Identify the cell.
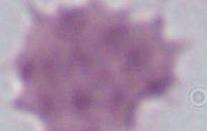
An erythrocyte.

Summary:
  - Magnification: 1000x
  - Modality: micrograph